Identify the blood parasite species.
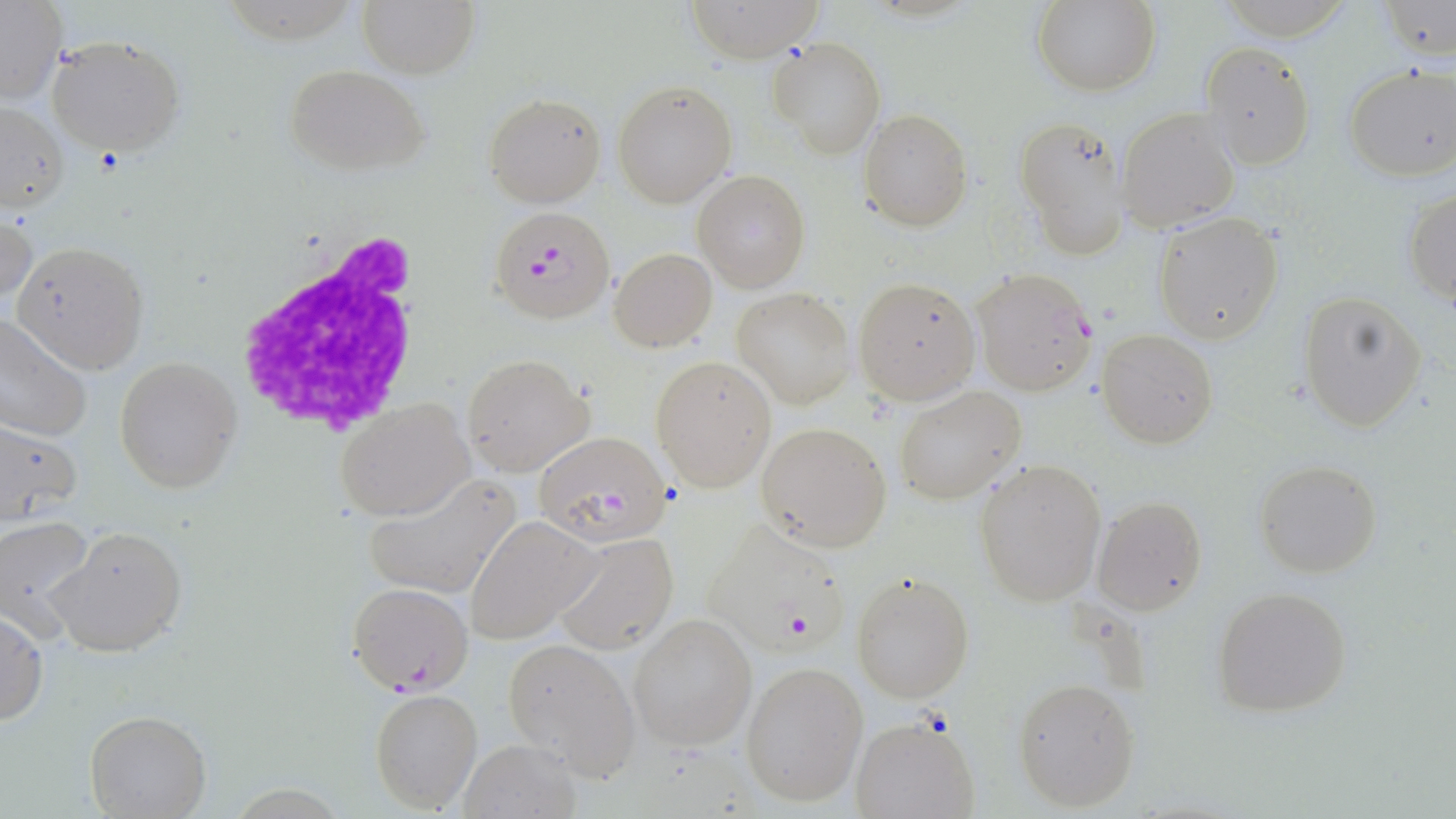

Plasmodium falciparum.

Approximate bounding boxes as (x1,y1)-(x2,y2) corner pairs in pixels. Plasmodium falciparum-infected red blood cell locations: (490,206)-(617,325), (970,268)-(1097,395), (533,430)-(674,545), (701,518)-(853,654), (347,581)-(472,695). Uninfected red blood cell locations: (358,0)-(479,77), (684,0)-(826,64), (1031,0)-(1160,96), (1379,2)-(1455,58), (0,3)-(67,104), (46,33)-(184,156), (768,38)-(884,157), (1200,42)-(1315,169), (282,64)-(429,176), (1344,64)-(1456,181), (612,79)-(737,209), (483,93)-(605,208), (0,103)-(68,213), (1118,108)-(1240,232), (859,109)-(971,230), (1014,120)-(1131,258), (694,170)-(809,292), (1403,188)-(1455,306), (1,211)-(38,309), (1153,212)-(1283,343), (13,241)-(148,374), (610,247)-(717,351), (852,277)-(980,405), (731,288)-(854,408), (1298,289)-(1426,433), (0,312)-(94,444), (1098,329)-(1218,447), (463,352)-(595,476), (114,356)-(240,492), (651,357)-(776,493), (892,385)-(1027,504), (334,396)-(474,521), (0,418)-(83,524), (756,421)-(892,552), (974,458)-(1107,608), (1253,459)-(1382,579), (362,471)-(523,600), (1091,495)-(1208,615), (0,515)-(97,639), (465,515)-(600,645), (49,526)-(187,658), (549,531)-(677,655), (850,569)-(976,704), (1211,585)-(1354,718), (0,610)-(47,727), (628,612)-(758,751), (502,636)-(642,780), (740,660)-(868,807), (1013,677)-(1142,812), (371,688)-(482,811), (84,710)-(211,818), (850,716)-(981,819), (457,737)-(583,818). White blood cell locations: (229,230)-(425,438). May-Grünwald-Giemsa stain. Single field of view. Thin blood smear. Optical microscopy. 1000x magnification. Image is 1456×819 pixels.